Comment on the morphology of the erythrocytes.
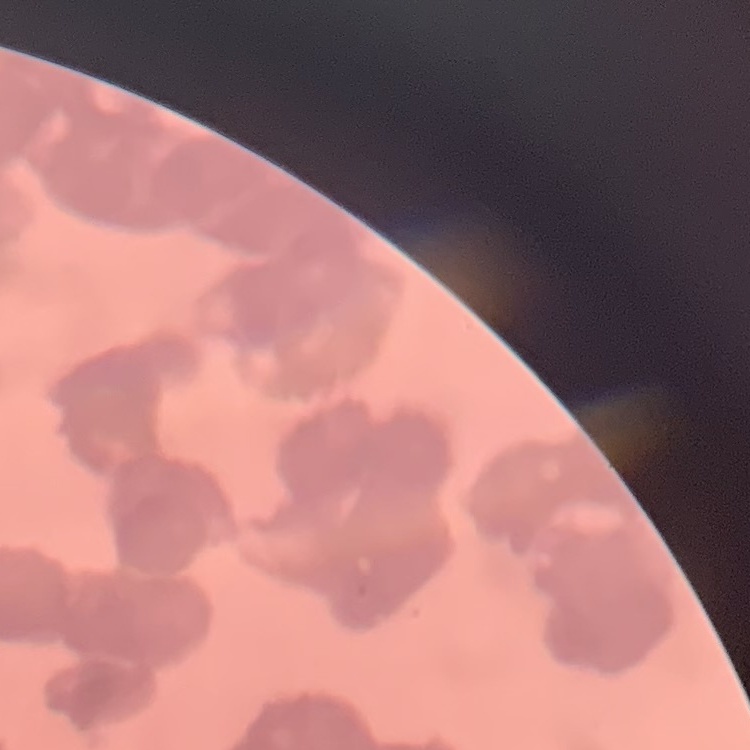

They show rouleaux formation.

Summary:
  - Image type: one tile cut from a larger photomicrograph
  - Preparation: thin blood smear
  - Stain: Field's or Giemsa